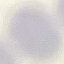

Summary:
  - Result: negative for malaria parasites
  - Capture: smartphone camera at the microscope eyepiece
  - Image type: automatically extracted cell patch, resized to 64 × 64 pixels
  - Stain: Giemsa
  - Preparation: thin blood smear